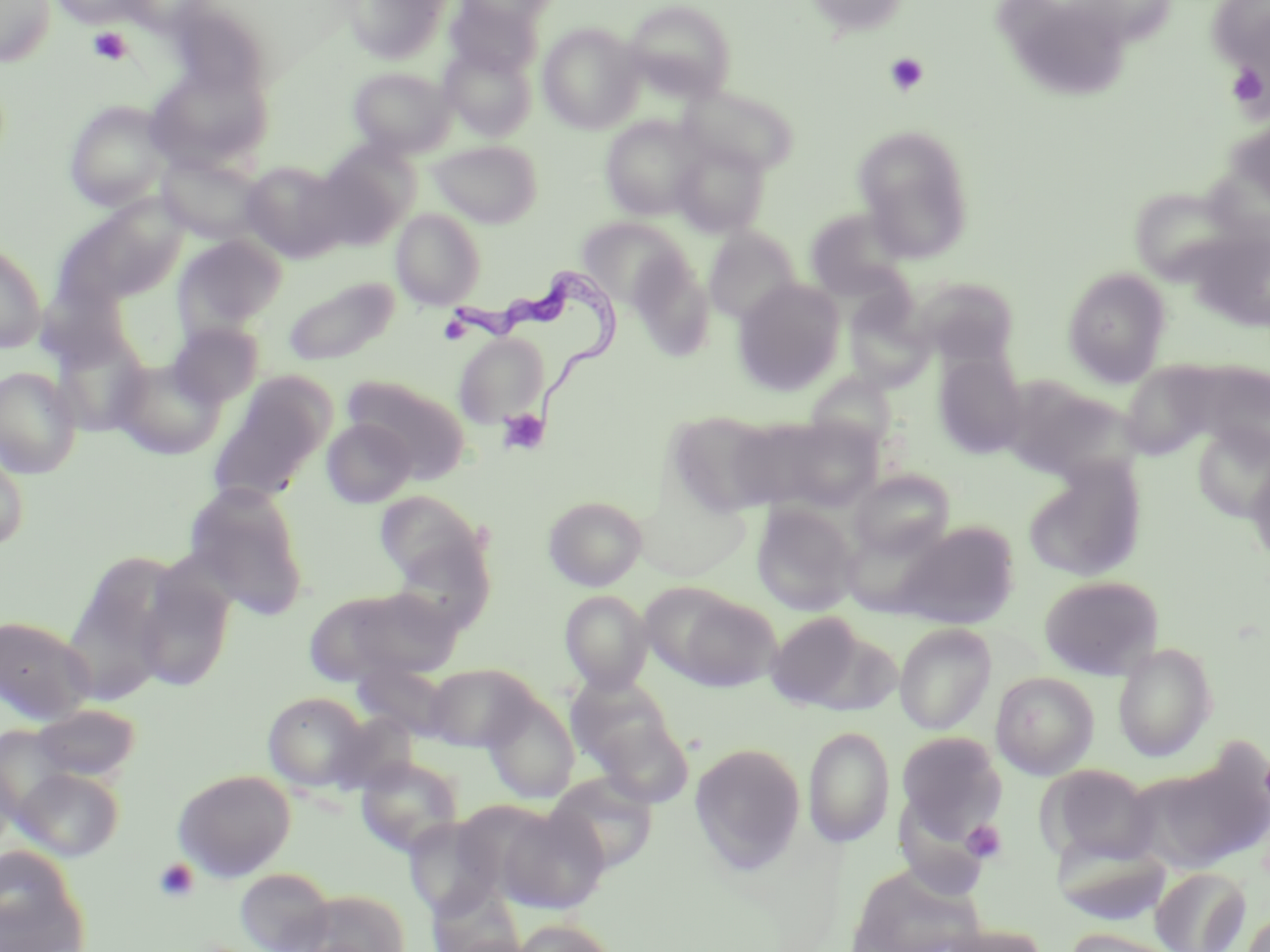 Approximate bounding boxes as named x1/y1/x2/y2 corners in pixels. Trypanosoma brucei locations: (x1=443, y1=270, x2=621, y2=419). Platelet locations: (x1=88, y1=27, x2=133, y2=65), (x1=883, y1=52, x2=929, y2=97), (x1=1225, y1=60, x2=1269, y2=117), (x1=497, y1=409, x2=550, y2=456), (x1=962, y1=819, x2=1008, y2=864), (x1=153, y1=858, x2=199, y2=903). Uninfected red blood cell locations: (x1=0, y1=0, x2=56, y2=67), (x1=51, y1=0, x2=150, y2=27), (x1=118, y1=0, x2=218, y2=34), (x1=345, y1=0, x2=452, y2=63), (x1=457, y1=0, x2=558, y2=30), (x1=624, y1=0, x2=737, y2=101), (x1=801, y1=0, x2=913, y2=38), (x1=444, y1=2, x2=541, y2=78), (x1=1011, y1=14, x2=1131, y2=98), (x1=537, y1=23, x2=645, y2=133), (x1=441, y1=44, x2=537, y2=140), (x1=145, y1=65, x2=272, y2=174), (x1=348, y1=67, x2=455, y2=158), (x1=680, y1=84, x2=800, y2=176), (x1=64, y1=100, x2=173, y2=211), (x1=600, y1=114, x2=706, y2=220), (x1=853, y1=124, x2=974, y2=261), (x1=672, y1=139, x2=769, y2=237), (x1=430, y1=140, x2=543, y2=228), (x1=315, y1=144, x2=418, y2=247), (x1=156, y1=153, x2=266, y2=245), (x1=242, y1=161, x2=349, y2=264), (x1=1129, y1=186, x2=1244, y2=285), (x1=59, y1=196, x2=190, y2=305), (x1=391, y1=208, x2=486, y2=310), (x1=805, y1=208, x2=912, y2=301), (x1=576, y1=217, x2=689, y2=309), (x1=704, y1=227, x2=801, y2=325), (x1=174, y1=234, x2=287, y2=337), (x1=1197, y1=241, x2=1270, y2=338), (x1=0, y1=243, x2=46, y2=353), (x1=628, y1=252, x2=716, y2=361), (x1=1062, y1=267, x2=1171, y2=386), (x1=282, y1=275, x2=399, y2=367), (x1=912, y1=275, x2=1020, y2=369), (x1=733, y1=279, x2=846, y2=395), (x1=843, y1=295, x2=935, y2=392), (x1=168, y1=321, x2=263, y2=408), (x1=51, y1=328, x2=151, y2=436), (x1=454, y1=333, x2=549, y2=427), (x1=934, y1=352, x2=1027, y2=458), (x1=110, y1=357, x2=225, y2=459), (x1=1127, y1=361, x2=1228, y2=453), (x1=0, y1=366, x2=82, y2=478), (x1=805, y1=371, x2=898, y2=454), (x1=342, y1=375, x2=471, y2=480), (x1=1002, y1=377, x2=1135, y2=484), (x1=208, y1=388, x2=324, y2=503), (x1=666, y1=410, x2=784, y2=516), (x1=755, y1=415, x2=888, y2=513), (x1=322, y1=418, x2=416, y2=508), (x1=1193, y1=423, x2=1270, y2=523), (x1=0, y1=444, x2=30, y2=552), (x1=1246, y1=456, x2=1270, y2=567), (x1=1023, y1=458, x2=1146, y2=583), (x1=849, y1=469, x2=955, y2=562), (x1=182, y1=481, x2=310, y2=619), (x1=633, y1=487, x2=752, y2=580), (x1=374, y1=491, x2=485, y2=585), (x1=543, y1=496, x2=647, y2=590), (x1=752, y1=503, x2=859, y2=615), (x1=887, y1=520, x2=1019, y2=630), (x1=83, y1=551, x2=183, y2=645), (x1=133, y1=568, x2=234, y2=693), (x1=1038, y1=575, x2=1165, y2=680), (x1=308, y1=585, x2=460, y2=686), (x1=657, y1=588, x2=780, y2=691), (x1=560, y1=590, x2=653, y2=693), (x1=63, y1=607, x2=169, y2=706), (x1=765, y1=612, x2=883, y2=713), (x1=0, y1=615, x2=96, y2=724), (x1=894, y1=623, x2=997, y2=734), (x1=1112, y1=641, x2=1218, y2=761), (x1=424, y1=662, x2=539, y2=751), (x1=353, y1=665, x2=453, y2=740), (x1=991, y1=672, x2=1099, y2=780), (x1=565, y1=675, x2=682, y2=781), (x1=263, y1=692, x2=370, y2=791), (x1=481, y1=693, x2=580, y2=804), (x1=31, y1=703, x2=142, y2=783), (x1=329, y1=713, x2=419, y2=795), (x1=590, y1=713, x2=694, y2=808), (x1=0, y1=726, x2=77, y2=821), (x1=803, y1=726, x2=895, y2=847), (x1=896, y1=732, x2=1006, y2=840), (x1=690, y1=742, x2=806, y2=873), (x1=1137, y1=748, x2=1269, y2=872), (x1=0, y1=754, x2=17, y2=857), (x1=355, y1=756, x2=464, y2=857), (x1=1044, y1=765, x2=1158, y2=866), (x1=13, y1=767, x2=126, y2=862), (x1=172, y1=769, x2=296, y2=882), (x1=546, y1=772, x2=658, y2=873), (x1=497, y1=805, x2=610, y2=914), (x1=403, y1=816, x2=503, y2=919), (x1=1054, y1=837, x2=1173, y2=927), (x1=1, y1=848, x2=90, y2=952), (x1=846, y1=862, x2=988, y2=952), (x1=234, y1=867, x2=336, y2=952), (x1=1150, y1=867, x2=1250, y2=952), (x1=301, y1=888, x2=412, y2=952), (x1=1241, y1=911, x2=1270, y2=952), (x1=509, y1=918, x2=621, y2=952), (x1=932, y1=922, x2=1049, y2=952), (x1=1062, y1=927, x2=1186, y2=952). Slide-level diagnosis: Trypanosoma brucei. Captured at 1000x magnification. Image is 1270×952 pixels. Thin blood smear. May-Grünwald-Giemsa stain. One field of a larger specimen. Light microscopy.